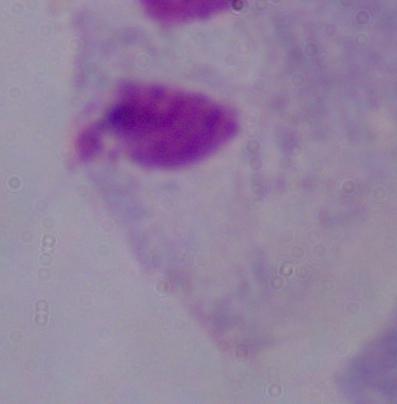

identification = trichomonad
modality = micrograph
magnification = 1000x